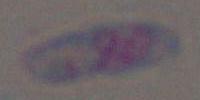

Toxoplasma gondii is shown. Photomicrograph. 1000x magnification.